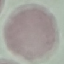
Result: no malaria parasites seen. Cell patch, automatically extracted from a larger field of view and resized to 64 × 64 pixels. Photographed with a smartphone camera at the microscope eyepiece. Giemsa-stained preparation. Thin blood smear.